Assess the morphology of the erythrocytes.
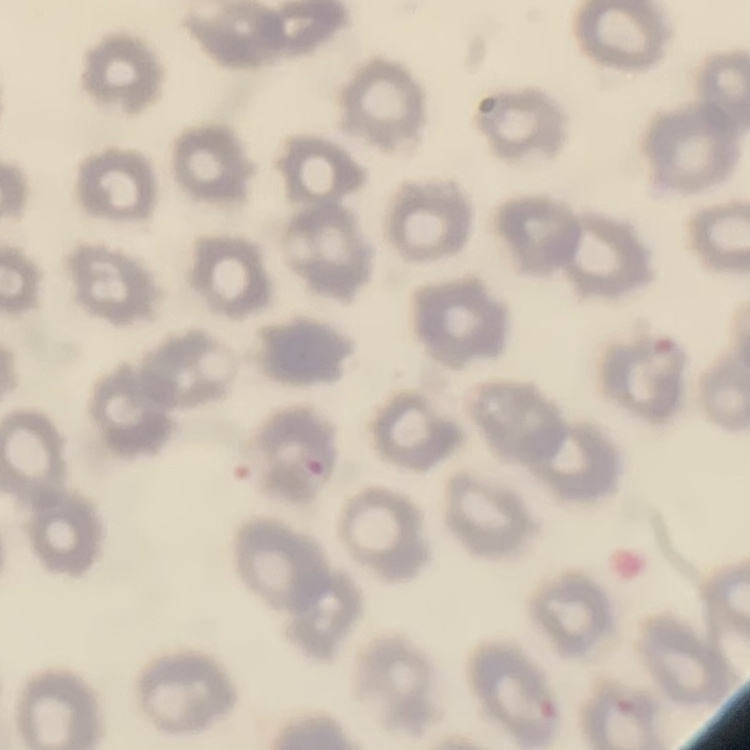

No rouleaux formation.

Thin blood film. One tile cut from a larger photomicrograph. Stained with either Field's or Giemsa.